Locate every leukocyte (white blood cell).
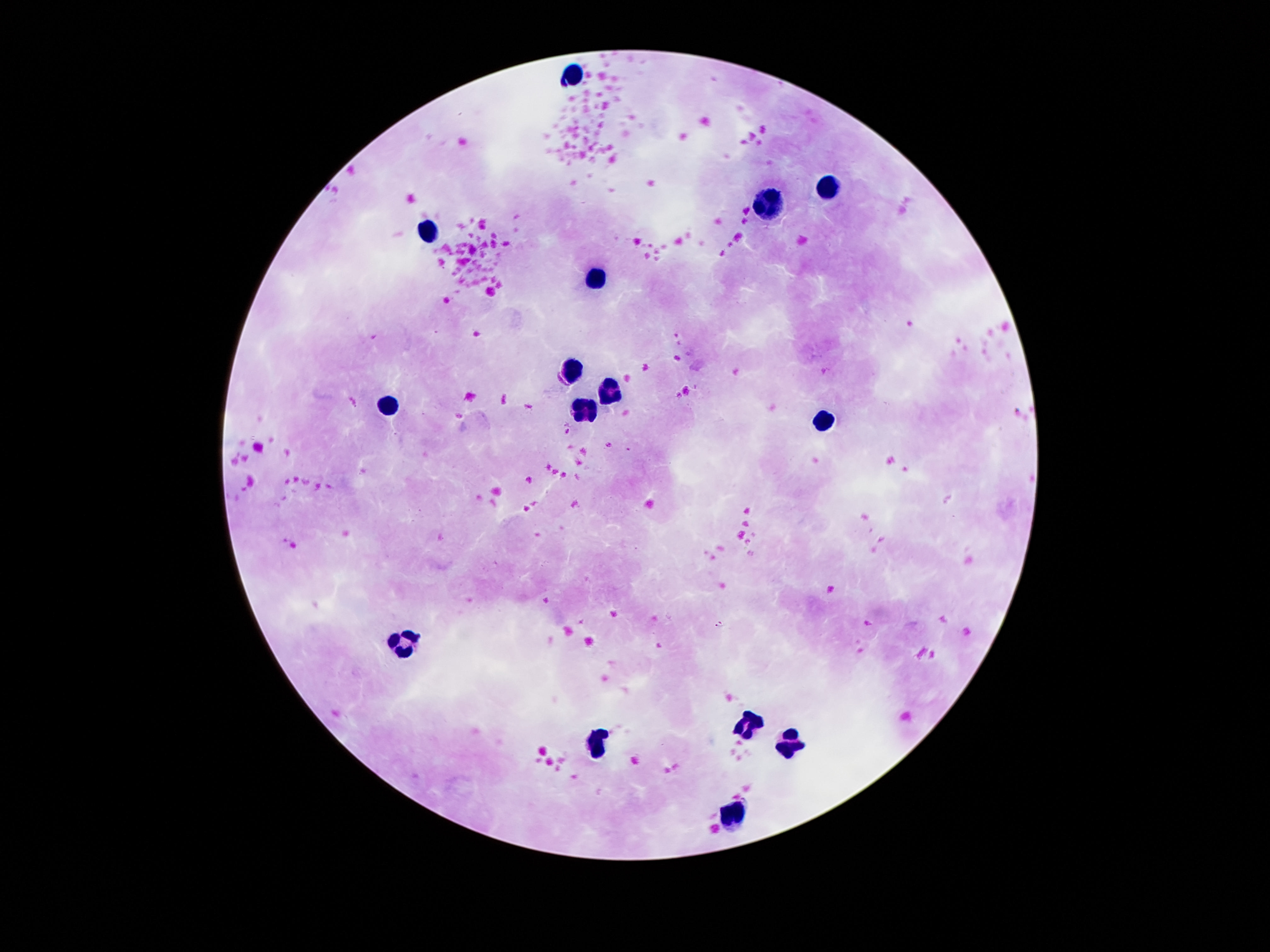
Approximate centers as (x, y) in pixels.
Leukocytes: (570, 77), (827, 190), (771, 204), (427, 233), (599, 276), (579, 373), (614, 390), (388, 409), (585, 409), (827, 423), (402, 643), (749, 724), (792, 743), (593, 744), (732, 817).

Summary:
  - Image size: 1270×952 pixels
  - Stain: Giemsa
  - Patient malaria status: not infected
  - Capture: smartphone camera through the microscope eyepiece
  - Preparation: thick blood film
  - Magnification: 100x
  - Field of view: single